Comment on the morphology of the erythrocytes.
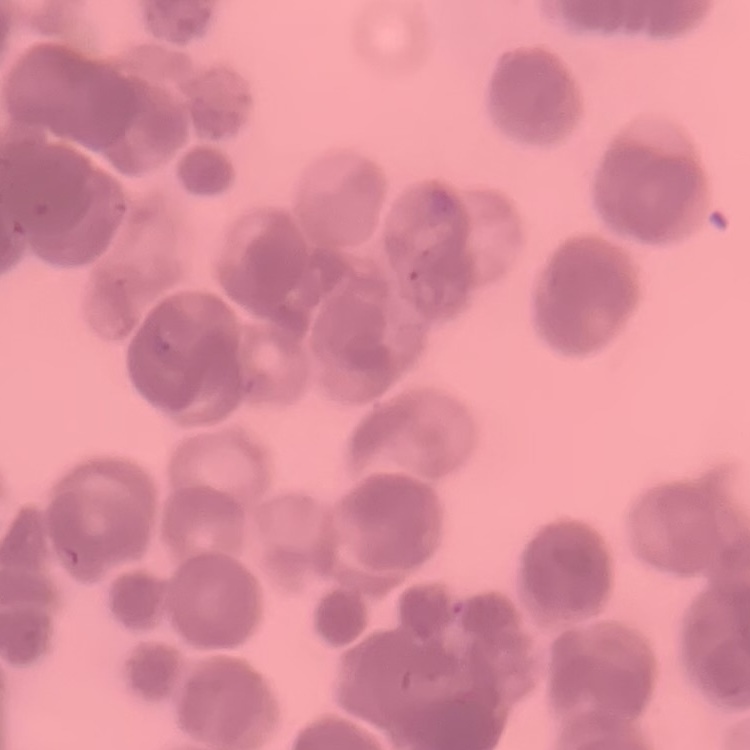

Rouleaux formation.

Summary:
  - Image type: one tile cut from a larger photomicrograph
  - Preparation: thin peripheral smear
  - Stain: Field's or Giemsa